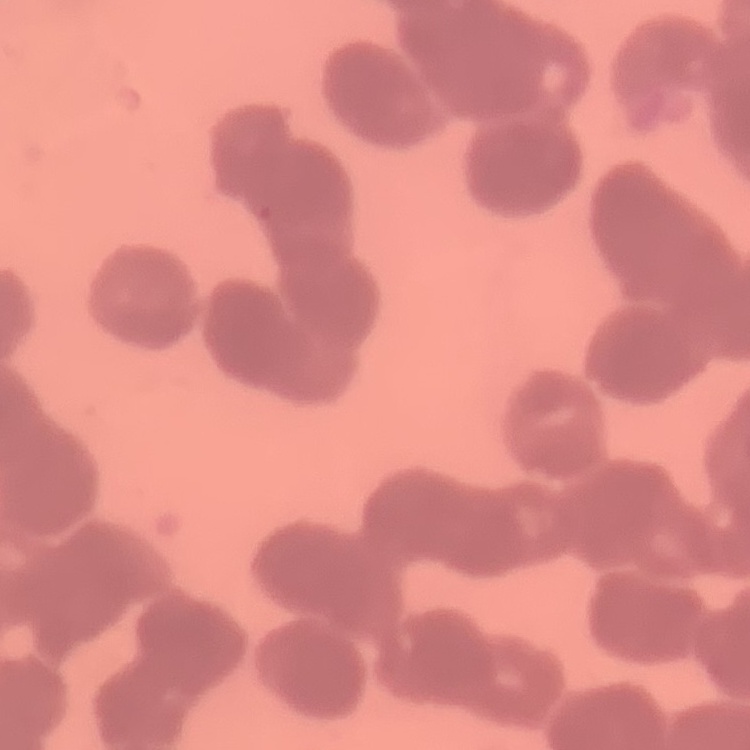 The red blood cells show rouleaux formation. Square crop of a larger photomicrograph. Stained with either Field's or Giemsa. Thin blood film.